Assess the morphology of the erythrocytes.
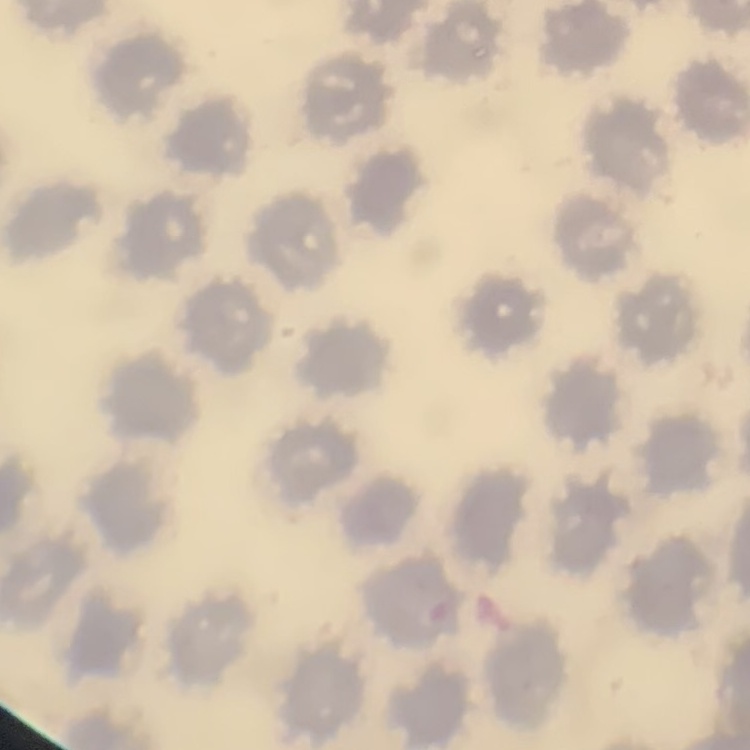
No rouleaux formation.

Summary:
  - Image type: square crop of a larger photomicrograph
  - Stain: Field's or Giemsa
  - Preparation: thin blood film